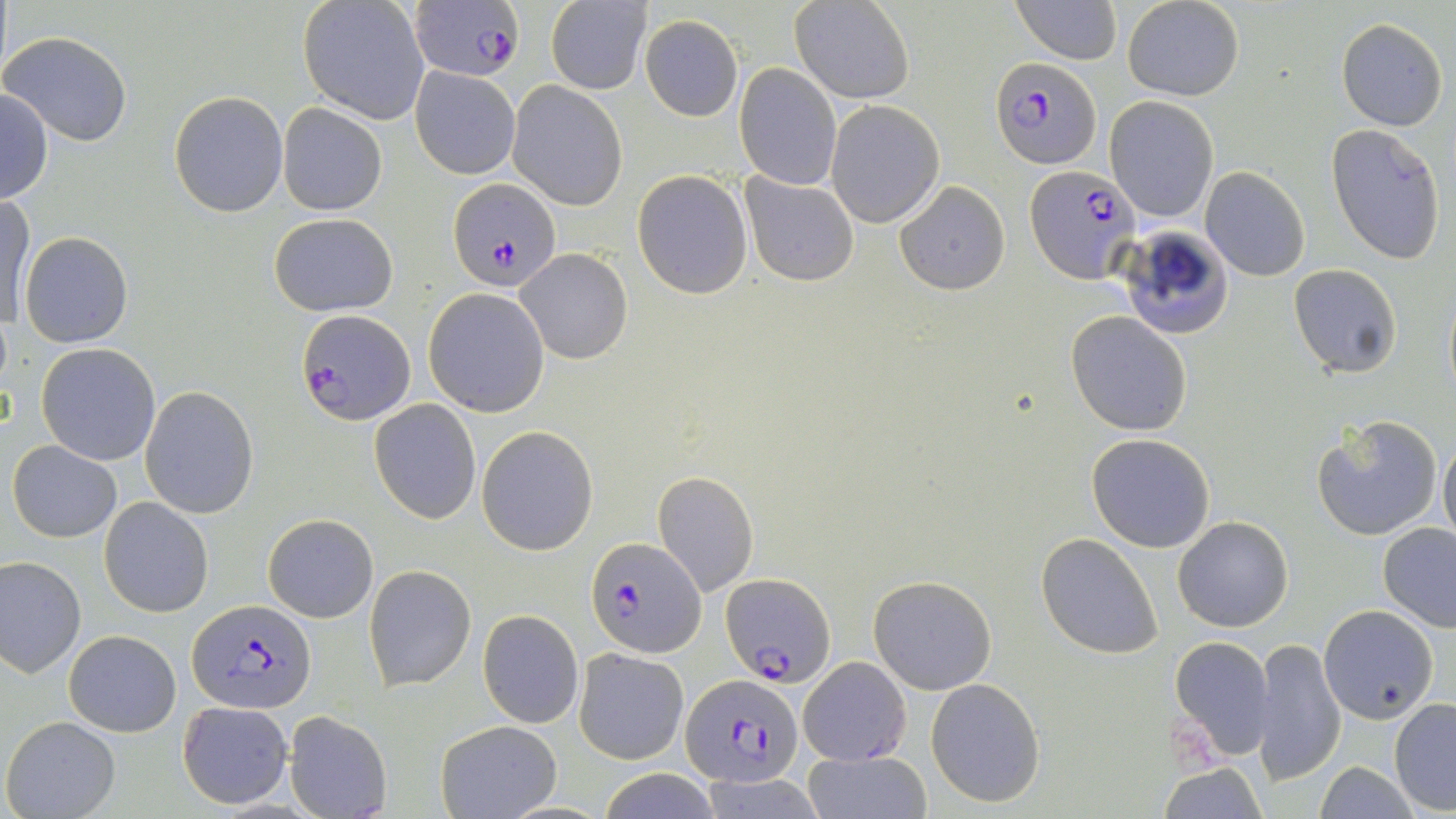
{
  "slide_level_diagnosis": "Plasmodium falciparum",
  "magnification": "1000x",
  "modality": "optical microscopy",
  "plasmodium_falciparum_infected_red_blood_cell_locations": "approximate bounding boxes as named x1/y1/x2/y2 corners in pixels: (x1=408, y1=4, x2=524, y2=81), (x1=990, y1=57, x2=1099, y2=168), (x1=1023, y1=164, x2=1141, y2=285), (x1=448, y1=180, x2=561, y2=291), (x1=297, y1=309, x2=414, y2=424), (x1=586, y1=537, x2=704, y2=659), (x1=722, y1=571, x2=836, y2=686), (x1=187, y1=599, x2=316, y2=713), (x1=680, y1=674, x2=803, y2=786)",
  "stain": "May-Grünwald-Giemsa",
  "field_of_view": "single",
  "uninfected_red_blood_cell_locations": "approximate bounding boxes as named x1/y1/x2/y2 corners in pixels: (x1=298, y1=0, x2=430, y2=124), (x1=546, y1=0, x2=651, y2=94), (x1=791, y1=0, x2=914, y2=103), (x1=1010, y1=0, x2=1123, y2=66), (x1=1123, y1=0, x2=1244, y2=101), (x1=641, y1=15, x2=743, y2=121), (x1=1337, y1=18, x2=1448, y2=131), (x1=2, y1=30, x2=134, y2=147), (x1=735, y1=63, x2=841, y2=189), (x1=410, y1=66, x2=520, y2=179), (x1=507, y1=80, x2=629, y2=211), (x1=0, y1=88, x2=52, y2=206), (x1=169, y1=91, x2=287, y2=217), (x1=1104, y1=96, x2=1218, y2=223), (x1=825, y1=100, x2=943, y2=226), (x1=278, y1=103, x2=387, y2=215), (x1=1326, y1=123, x2=1448, y2=265), (x1=1199, y1=167, x2=1310, y2=281), (x1=632, y1=169, x2=753, y2=298), (x1=741, y1=173, x2=858, y2=285), (x1=893, y1=180, x2=1011, y2=295), (x1=1, y1=193, x2=34, y2=327), (x1=269, y1=212, x2=398, y2=316), (x1=1121, y1=226, x2=1233, y2=342), (x1=20, y1=231, x2=133, y2=348), (x1=516, y1=248, x2=632, y2=364), (x1=1287, y1=264, x2=1402, y2=379), (x1=1442, y1=282, x2=1455, y2=402), (x1=423, y1=289, x2=549, y2=416), (x1=1066, y1=310, x2=1192, y2=435), (x1=36, y1=343, x2=162, y2=465), (x1=140, y1=386, x2=259, y2=518), (x1=369, y1=400, x2=482, y2=522), (x1=1310, y1=414, x2=1443, y2=542), (x1=476, y1=427, x2=598, y2=555), (x1=1438, y1=433, x2=1456, y2=547), (x1=1087, y1=434, x2=1216, y2=553), (x1=8, y1=441, x2=123, y2=542), (x1=652, y1=470, x2=759, y2=598), (x1=99, y1=496, x2=213, y2=617), (x1=263, y1=512, x2=378, y2=622), (x1=1172, y1=516, x2=1293, y2=632), (x1=1378, y1=522, x2=1456, y2=631), (x1=1036, y1=533, x2=1163, y2=660), (x1=1, y1=555, x2=86, y2=676), (x1=366, y1=564, x2=475, y2=690), (x1=868, y1=574, x2=998, y2=695), (x1=1318, y1=604, x2=1439, y2=722), (x1=477, y1=609, x2=583, y2=728), (x1=64, y1=630, x2=181, y2=737), (x1=1169, y1=636, x2=1274, y2=760), (x1=1254, y1=638, x2=1345, y2=783), (x1=573, y1=647, x2=689, y2=764), (x1=797, y1=656, x2=913, y2=767), (x1=925, y1=678, x2=1046, y2=808), (x1=1389, y1=699, x2=1456, y2=814), (x1=177, y1=701, x2=294, y2=809), (x1=284, y1=709, x2=393, y2=819), (x1=3, y1=716, x2=121, y2=818), (x1=434, y1=720, x2=561, y2=818), (x1=802, y1=750, x2=932, y2=819), (x1=1313, y1=761, x2=1418, y2=819), (x1=1158, y1=762, x2=1270, y2=817), (x1=594, y1=768, x2=725, y2=819)",
  "image_size": "1456×819 pixels",
  "preparation": "thin blood film"
}